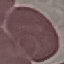
result = negative for malaria parasites
image type = automatically extracted cell patch, resized to 64 × 64 pixels
stain = Giemsa
preparation = thin smear
capture = smartphone through the microscope eyepiece